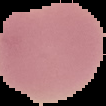

{
  "preparation": "thin blood smear",
  "image_type": "segmented cell region on a black background",
  "image_size": "106×106 pixels",
  "malaria_status": "uninfected"
}